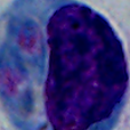

A leukocyte is shown. Photomicrograph. Captured at 1000x magnification.